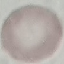

Summary:
  - Result: no malaria parasites seen
  - Image type: automatically extracted cell patch, resized to 64 × 64 pixels
  - Preparation: thin blood film
  - Capture: smartphone camera at the microscope eyepiece
  - Stain: Giemsa